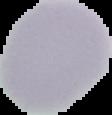
Summary:
  - Preparation: thin blood film
  - Image size: 112×115 pixels
  - Result: negative for malaria parasites
  - Image type: segmented cell region on a black background